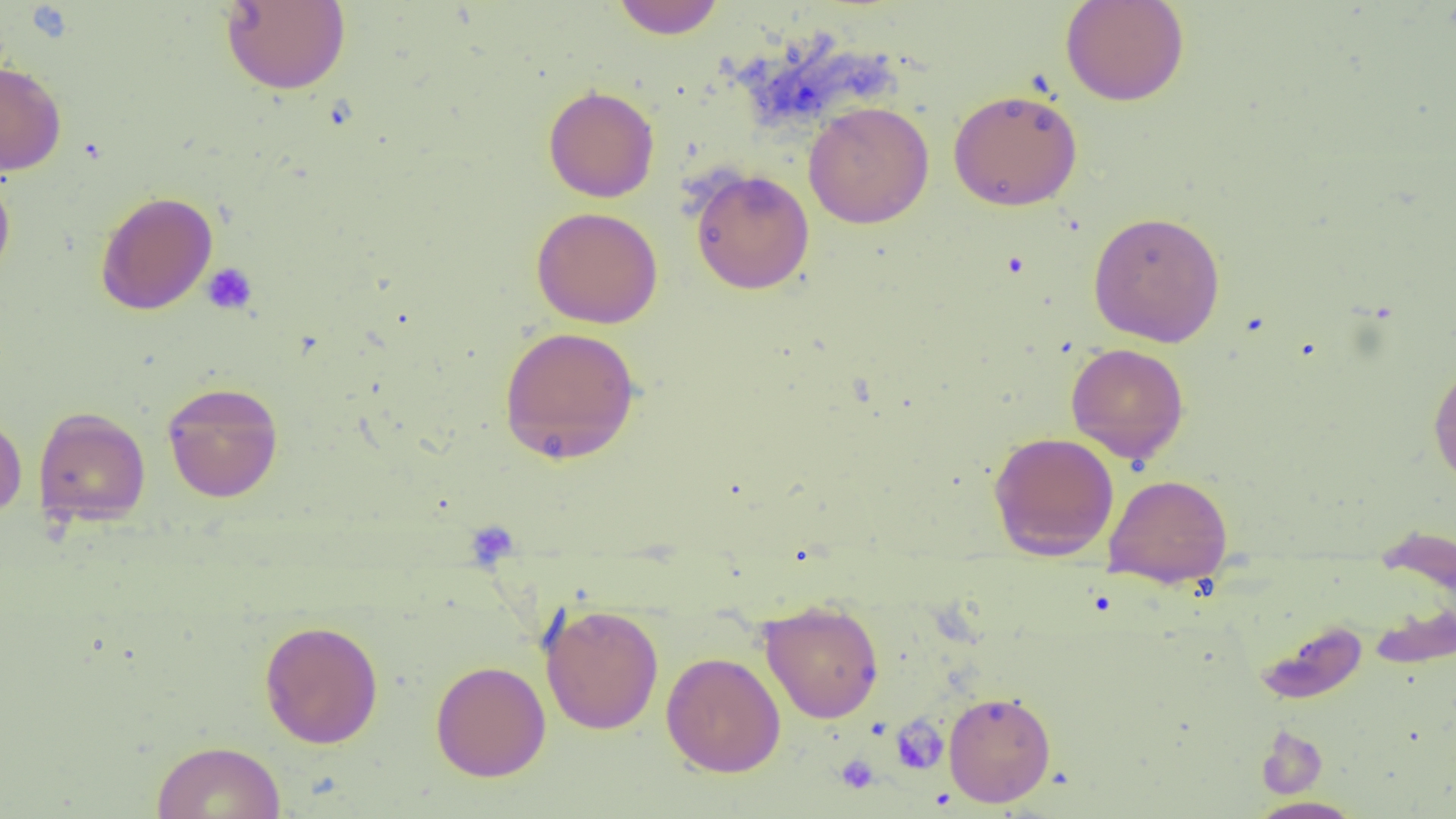
Approximate bounding boxes as [x1, y1, x2, y2] in pixels. Platelet locations: [25, 3, 74, 43], [202, 263, 258, 315], [465, 520, 519, 571], [890, 717, 949, 775], [835, 754, 879, 794]. Uninfected red blood cell locations: [1060, 0, 1190, 107], [221, 1, 351, 95], [610, 1, 726, 39], [0, 59, 67, 175], [542, 84, 659, 203], [948, 88, 1083, 211], [804, 101, 934, 229], [0, 165, 16, 286], [690, 168, 815, 294], [95, 190, 218, 316], [531, 206, 664, 328], [1088, 210, 1226, 347], [498, 326, 641, 464], [1066, 343, 1189, 464], [1427, 359, 1456, 490], [162, 382, 283, 503], [33, 406, 151, 527], [0, 411, 27, 522], [988, 431, 1120, 561], [1104, 473, 1232, 588], [759, 600, 884, 724], [540, 603, 664, 735], [1255, 619, 1369, 704], [258, 620, 384, 748], [661, 652, 786, 777], [430, 660, 551, 781], [943, 690, 1056, 807], [1256, 725, 1328, 799], [150, 740, 286, 819], [1247, 796, 1366, 818]. Slide-level diagnosis: negative for blood parasites. Optical microscopy. Thin blood film. Image is 1456×819 pixels. Single field of view. Captured at 1000x magnification.